Classify this cell by malaria status.
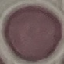
It is uninfected.

Summary:
  - Preparation: thin blood smear
  - Capture: smartphone through the microscope eyepiece
  - Stain: Giemsa
  - Image type: automatically extracted cell patch, resized to 64 × 64 pixels